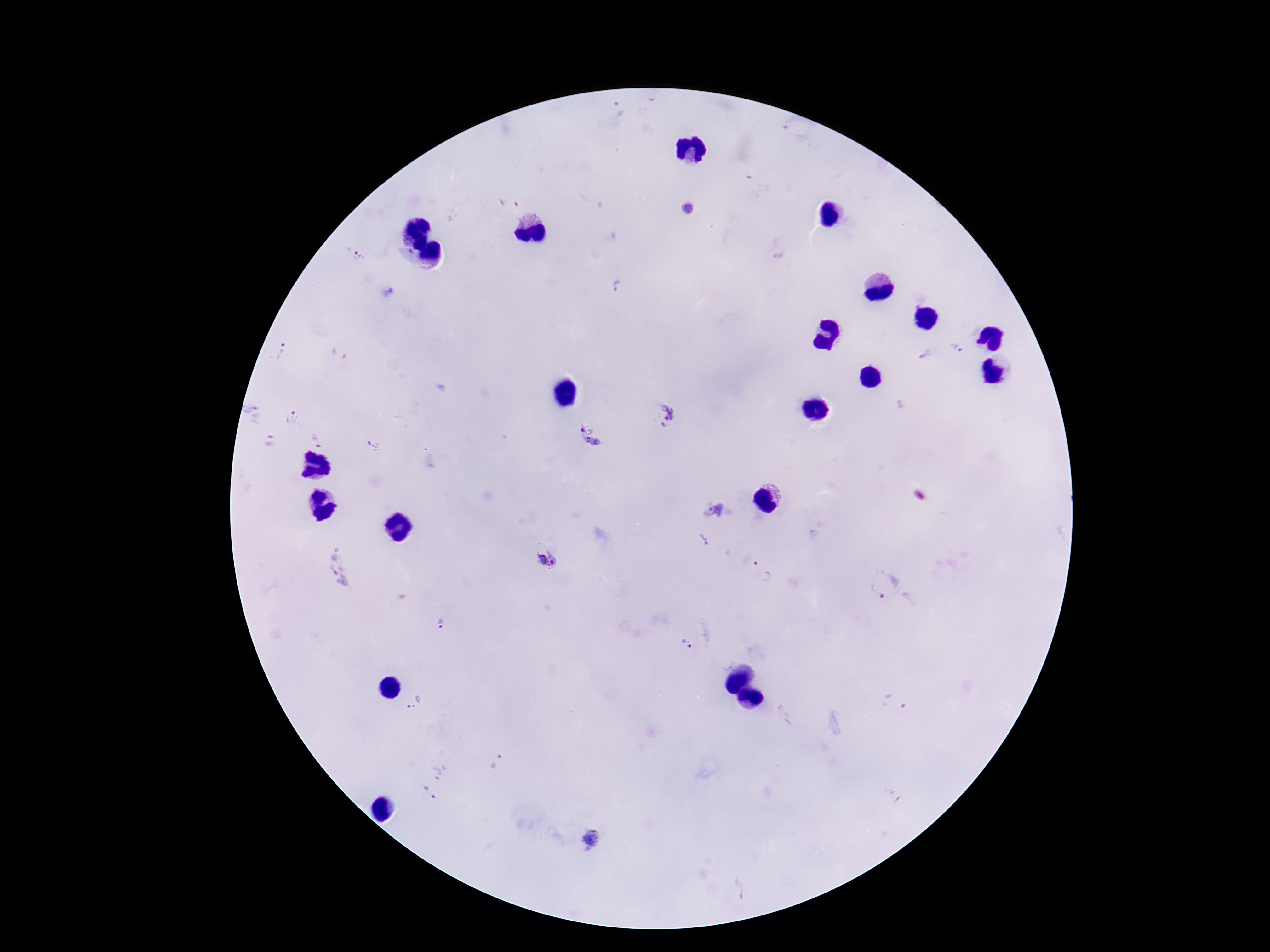
Approximate centers as (x, y) in pixels.
Summary:
  - Plasmodium parasite locations: (618, 108), (508, 202), (689, 209), (357, 254), (616, 284), (957, 347), (280, 352), (341, 354), (925, 354), (253, 411), (662, 415), (293, 418), (590, 436), (316, 441), (270, 442), (372, 445), (713, 510), (704, 539), (549, 559), (338, 566), (763, 572), (885, 584), (441, 624), (686, 644), (415, 704), (896, 705), (499, 762), (434, 781), (593, 839), (738, 889)
  - Capture: smartphone camera through the microscope eyepiece
  - Field of view: one from this slide
  - Magnification: 100x
  - Preparation: thick blood film
  - Image size: 1270×952 pixels
  - Patient malaria status: infected
  - Stain: Giemsa